Give the preparation type.
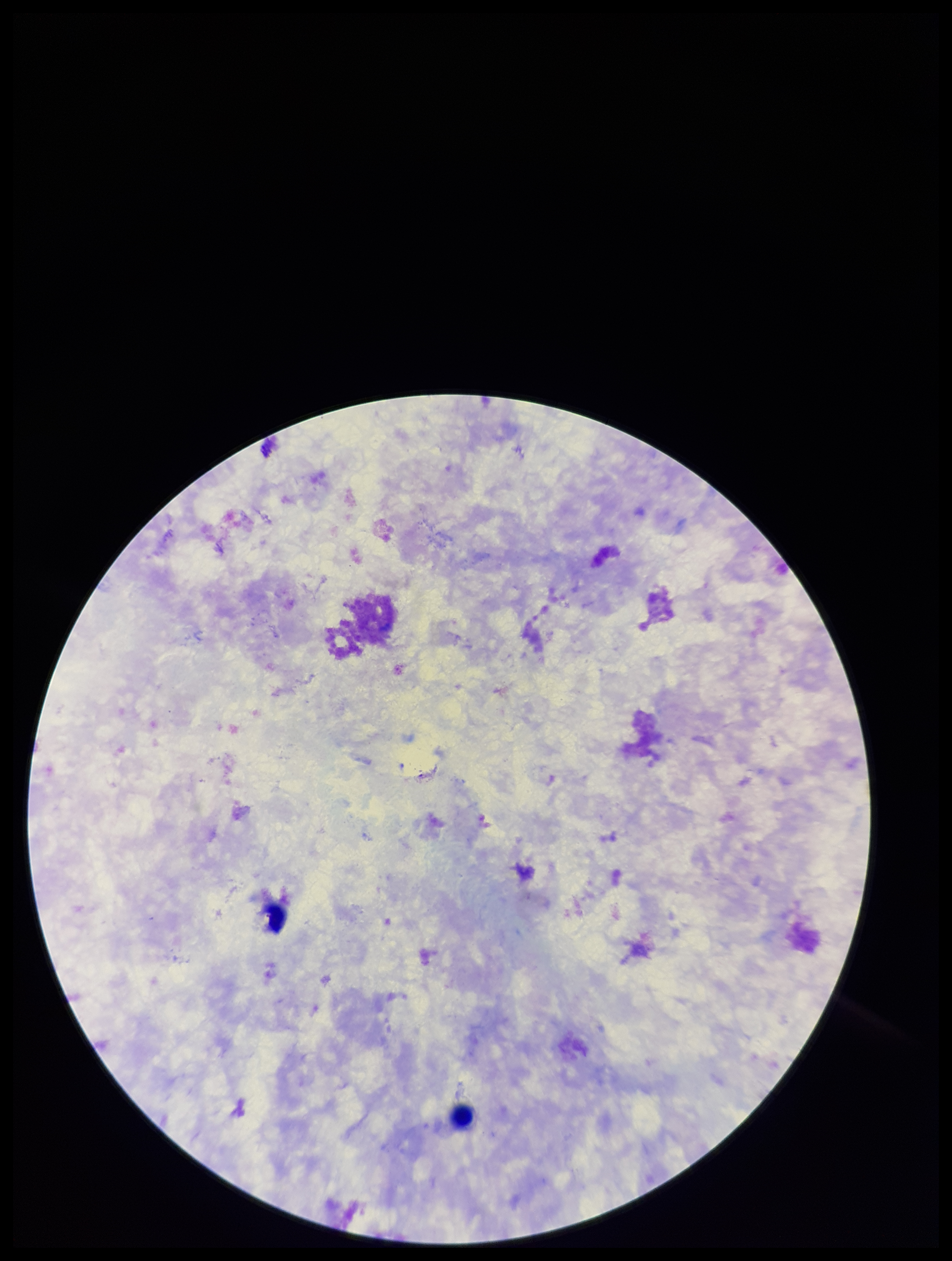
It is a thick blood smear.

Summary:
  - Capture: smartphone photograph through the microscope eyepiece
  - Parasite count: 0
  - Field of view: one from this slide
  - Patient malaria status: negative
  - Plasmodium parasites: none detected
  - Leukocyte count: 2
  - Stain: Giemsa
  - Image size: 952×1261 pixels